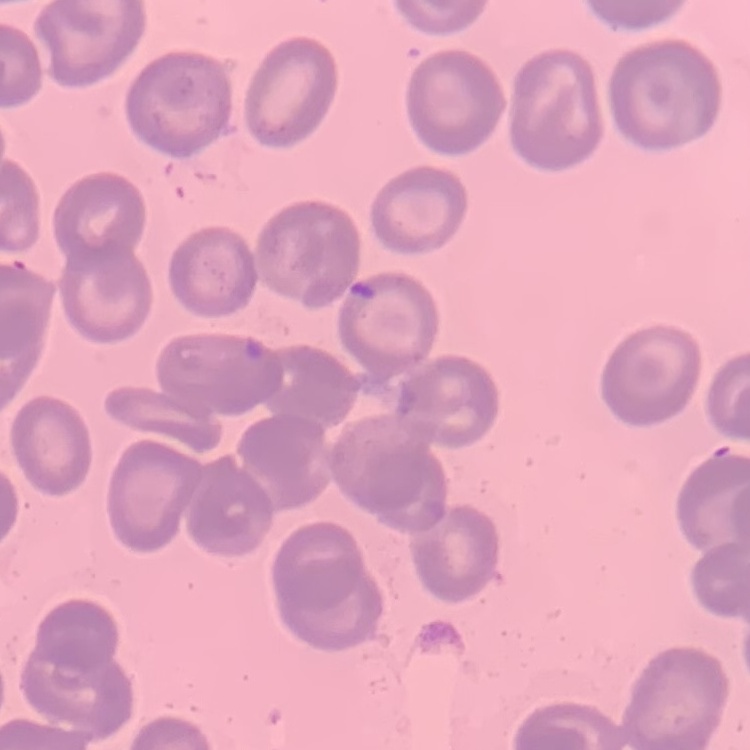

The erythrocytes show no rouleaux formation. Thin blood film. One tile cut from a larger photomicrograph. Field's or Giemsa stain.